Report the malaria status of this cell.
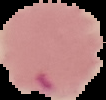

Parasitized.

Image is 106×100 pixels. Cell region segmented out of the field of view; the surrounding area is masked to black. From a thin blood film.